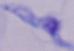
Summary:
  - Identification: trypanosome
  - Modality: micrograph
  - Magnification: 1000x